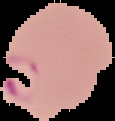

Summary:
  - Result: malaria parasites identified
  - Image size: 115×121 pixels
  - Image type: segmented cell region with the area outside set to black
  - Preparation: thin blood smear